Assess the morphology of the red blood cells.
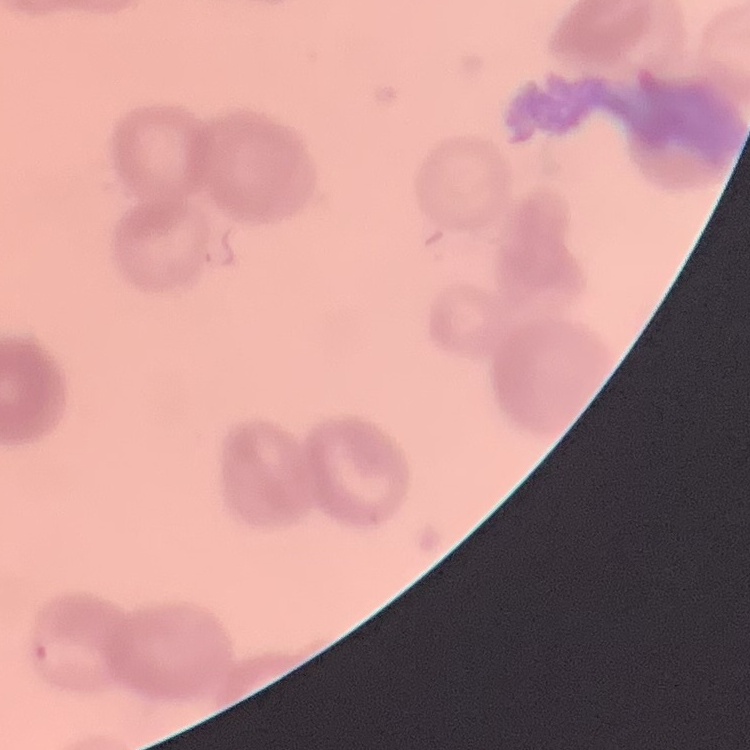

Rouleaux formation.

Summary:
  - Image type: one tile cut from a larger photomicrograph
  - Stain: Field's or Giemsa
  - Preparation: thin blood film